Assess this cell for malaria.
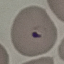
It is parasitized.

capture = smartphone camera at the microscope eyepiece
preparation = thin blood smear
stain = Giemsa
image type = automatically extracted cell patch, resized to 64 × 64 pixels